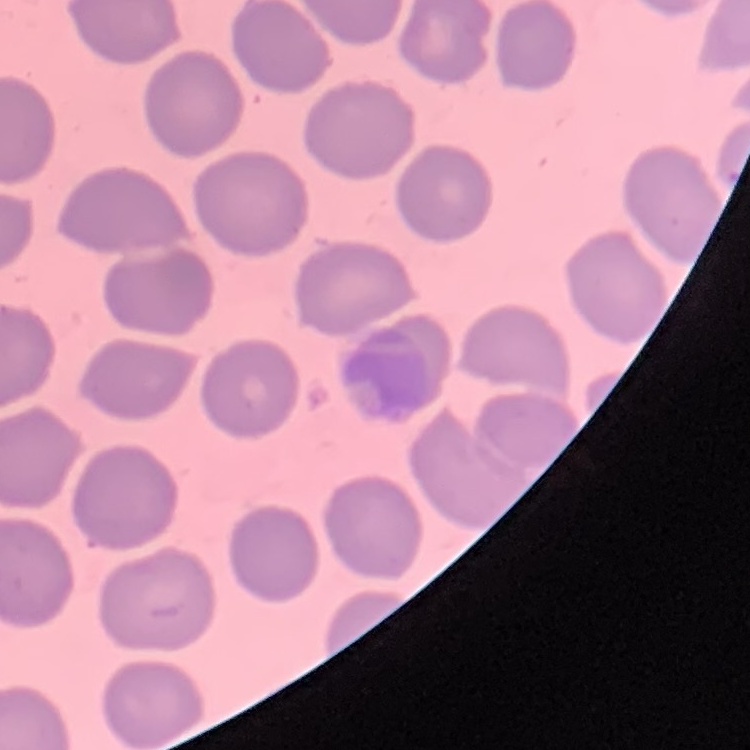 The red blood cells show no rouleaux formation. Thin peripheral smear. One tile cut from a larger photomicrograph. Field's or Giemsa stain.